State which parasite is depicted.
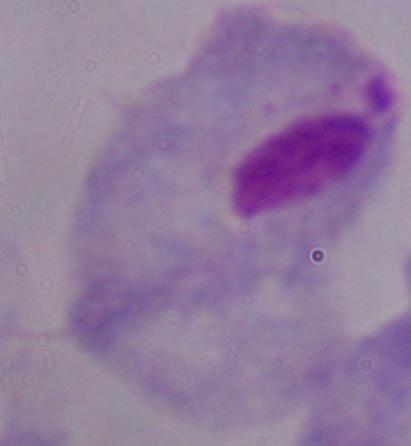

This is a trichomonad.

{
  "modality": "micrograph",
  "magnification": "1000x"
}